Identify the blood parasite species.
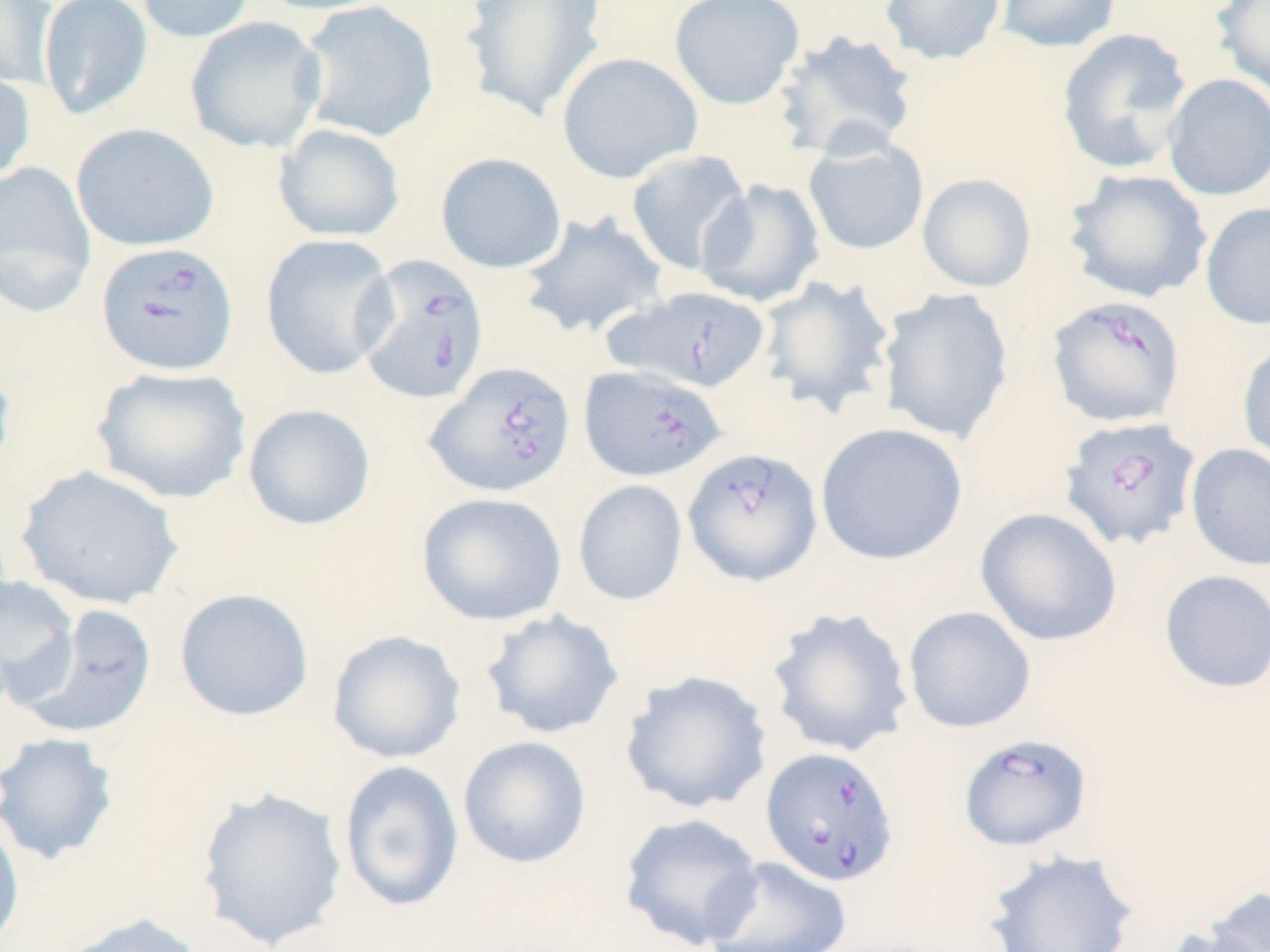
Babesia divergens.

Approximate bounding boxes as named x1/y1/x2/y2 corners in pixels. Uninfected red blood cell locations: (x1=37, y1=0, x2=154, y2=121), (x1=132, y1=0, x2=258, y2=44), (x1=252, y1=0, x2=400, y2=16), (x1=295, y1=0, x2=439, y2=143), (x1=459, y1=0, x2=608, y2=122), (x1=669, y1=0, x2=805, y2=110), (x1=879, y1=0, x2=1006, y2=66), (x1=994, y1=0, x2=1121, y2=54), (x1=1212, y1=0, x2=1270, y2=99), (x1=0, y1=1, x2=58, y2=90), (x1=184, y1=16, x2=328, y2=153), (x1=1056, y1=28, x2=1193, y2=175), (x1=775, y1=29, x2=919, y2=161), (x1=556, y1=51, x2=703, y2=184), (x1=0, y1=67, x2=36, y2=187), (x1=1162, y1=73, x2=1270, y2=201), (x1=70, y1=122, x2=220, y2=252), (x1=273, y1=123, x2=406, y2=242), (x1=802, y1=138, x2=930, y2=255), (x1=625, y1=148, x2=754, y2=277), (x1=435, y1=152, x2=567, y2=274), (x1=0, y1=161, x2=97, y2=316), (x1=1064, y1=168, x2=1212, y2=303), (x1=917, y1=173, x2=1038, y2=293), (x1=696, y1=178, x2=825, y2=308), (x1=1201, y1=201, x2=1270, y2=331), (x1=518, y1=211, x2=669, y2=340), (x1=260, y1=234, x2=399, y2=380), (x1=757, y1=275, x2=895, y2=418), (x1=878, y1=287, x2=1014, y2=445), (x1=1236, y1=340, x2=1270, y2=470), (x1=0, y1=356, x2=16, y2=484), (x1=92, y1=365, x2=252, y2=505), (x1=242, y1=403, x2=377, y2=530), (x1=815, y1=422, x2=969, y2=566), (x1=1186, y1=444, x2=1270, y2=571), (x1=16, y1=464, x2=184, y2=610), (x1=573, y1=479, x2=689, y2=606), (x1=417, y1=491, x2=568, y2=626), (x1=975, y1=507, x2=1122, y2=647), (x1=1159, y1=569, x2=1270, y2=694), (x1=0, y1=573, x2=80, y2=707), (x1=174, y1=588, x2=314, y2=721), (x1=15, y1=604, x2=158, y2=738), (x1=903, y1=605, x2=1037, y2=734), (x1=765, y1=606, x2=915, y2=758), (x1=479, y1=609, x2=624, y2=740), (x1=326, y1=629, x2=467, y2=764), (x1=619, y1=670, x2=772, y2=815), (x1=0, y1=731, x2=119, y2=866), (x1=457, y1=736, x2=592, y2=869), (x1=338, y1=760, x2=465, y2=913), (x1=195, y1=786, x2=348, y2=950), (x1=0, y1=810, x2=25, y2=952), (x1=618, y1=812, x2=765, y2=951), (x1=983, y1=847, x2=1140, y2=952), (x1=703, y1=856, x2=852, y2=952), (x1=1201, y1=886, x2=1270, y2=951), (x1=57, y1=912, x2=208, y2=952), (x1=1159, y1=925, x2=1267, y2=952). Babesia divergens-infected red blood cell locations: (x1=95, y1=241, x2=239, y2=377), (x1=354, y1=254, x2=490, y2=405), (x1=605, y1=284, x2=772, y2=393), (x1=1047, y1=295, x2=1186, y2=428), (x1=425, y1=361, x2=576, y2=497), (x1=579, y1=364, x2=727, y2=483), (x1=1058, y1=415, x2=1202, y2=552), (x1=683, y1=447, x2=822, y2=587), (x1=957, y1=732, x2=1093, y2=853), (x1=761, y1=746, x2=899, y2=887). Thin blood film. May-Grünwald-Giemsa-stained preparation. Captured at 1000x magnification. Optical microscopy. Image is 1270×952 pixels. One field of a larger specimen.